Name the parasite shown.
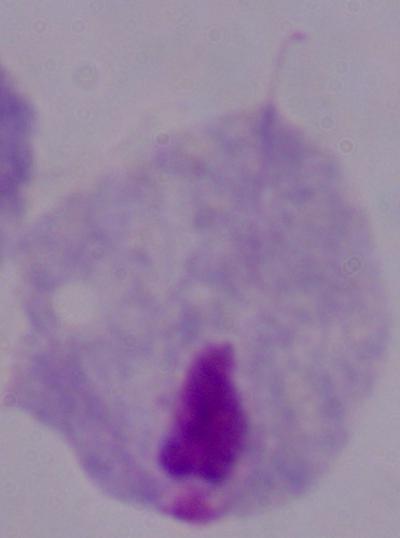

This is a trichomonad.

Summary:
  - Modality: photomicrograph
  - Magnification: 1000x